Classify this cell by malaria status.
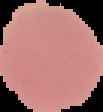
It is uninfected.

Segmented cell region on a black background. Image is 103×112 pixels. From a thin blood film.